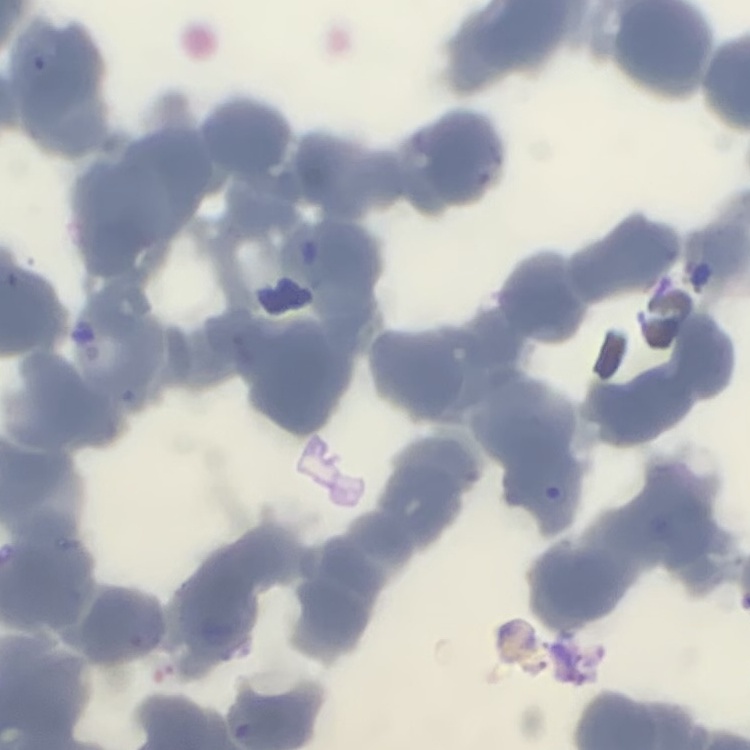

erythrocyte morphology = rouleaux formation
image type = one tile cut from a larger photomicrograph
preparation = thin blood smear
stain = Field's or Giemsa